Locate the Plasmodium falciparum-infected red blood cells and any of indeterminate infection status.
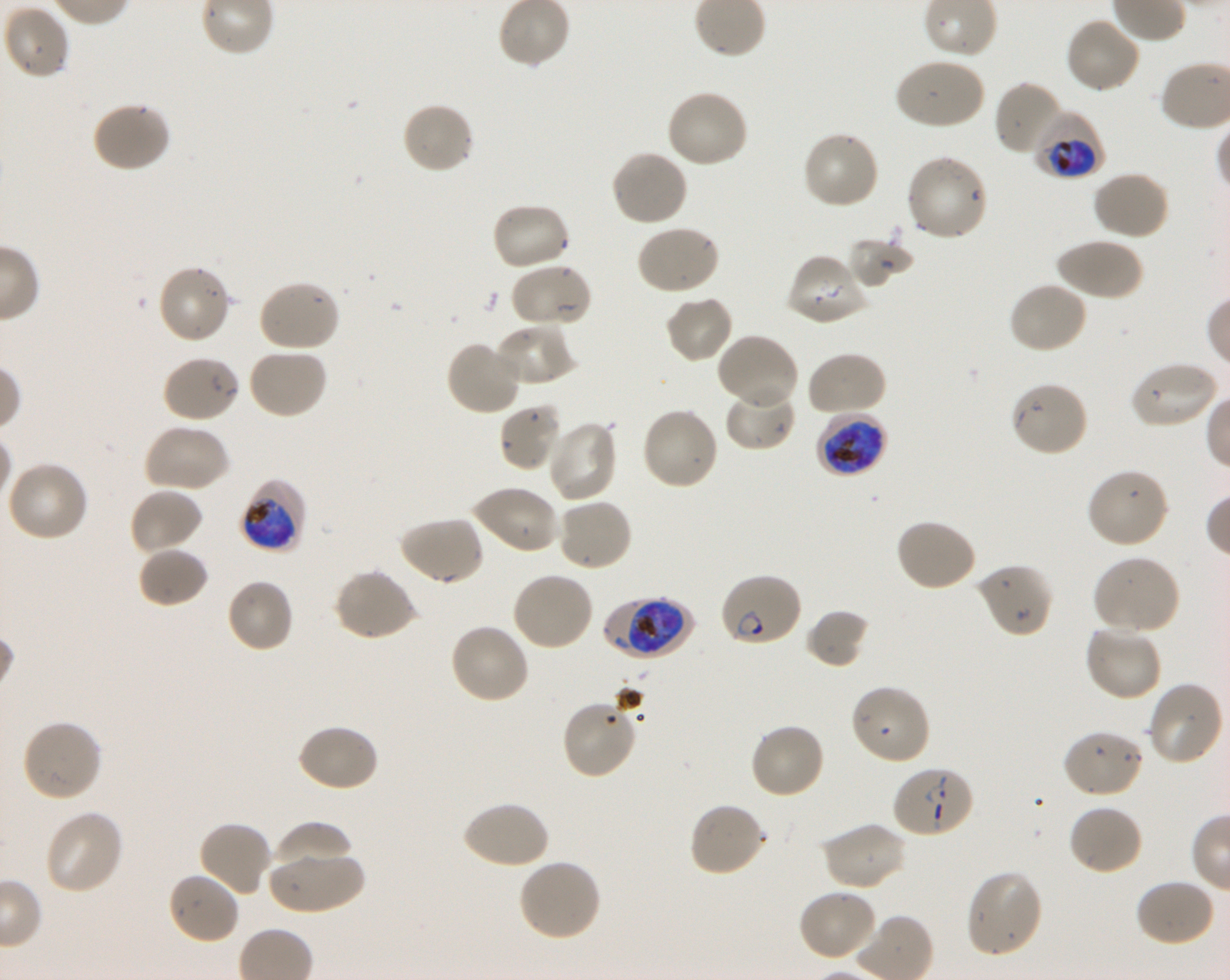
Approximate bounding rectangles given as corner coordinates in pixels from the top-left. Not every red blood cell is marked. A life-cycle stage — or a range of stages, where the recorded stages span more than one — follows each staged infected red blood cell.
Infected red blood cells: (x1=1032, y1=110, x2=1108, y2=180) trophozoite; (x1=815, y1=411, x2=888, y2=478) late trophozoite to late schizont; (x1=240, y1=482, x2=305, y2=551) early trophozoite to early schizont; (x1=717, y1=572, x2=802, y2=648) ring; (x1=603, y1=594, x2=693, y2=660) early trophozoite to early schizont; (x1=891, y1=764, x2=975, y2=839) ring.
No red blood cells of indeterminate infection status observed.

Summary:
  - Locations of uninfected red blood cells: (x1=3, y1=4, x2=70, y2=80), (x1=1064, y1=15, x2=1142, y2=95), (x1=894, y1=57, x2=986, y2=131), (x1=993, y1=80, x2=1065, y2=157), (x1=665, y1=90, x2=750, y2=169), (x1=92, y1=101, x2=172, y2=174), (x1=401, y1=101, x2=475, y2=176), (x1=800, y1=131, x2=881, y2=211), (x1=610, y1=149, x2=689, y2=228), (x1=905, y1=154, x2=988, y2=242), (x1=1091, y1=170, x2=1170, y2=241), (x1=489, y1=202, x2=572, y2=272), (x1=636, y1=224, x2=721, y2=296), (x1=1055, y1=236, x2=1143, y2=302), (x1=847, y1=237, x2=914, y2=288), (x1=785, y1=251, x2=870, y2=326), (x1=510, y1=263, x2=593, y2=330), (x1=156, y1=264, x2=232, y2=345), (x1=257, y1=279, x2=341, y2=353), (x1=1007, y1=281, x2=1089, y2=355), (x1=664, y1=293, x2=734, y2=364), (x1=493, y1=324, x2=574, y2=386), (x1=716, y1=333, x2=800, y2=411), (x1=446, y1=339, x2=523, y2=416), (x1=246, y1=348, x2=329, y2=420), (x1=805, y1=351, x2=887, y2=418), (x1=160, y1=354, x2=240, y2=424), (x1=1127, y1=360, x2=1219, y2=430), (x1=1009, y1=380, x2=1090, y2=457), (x1=724, y1=385, x2=796, y2=451), (x1=498, y1=401, x2=565, y2=473), (x1=640, y1=406, x2=721, y2=492), (x1=545, y1=419, x2=619, y2=503), (x1=142, y1=424, x2=230, y2=493), (x1=5, y1=460, x2=89, y2=543), (x1=1087, y1=468, x2=1170, y2=549), (x1=469, y1=485, x2=559, y2=555), (x1=128, y1=487, x2=203, y2=555), (x1=555, y1=497, x2=633, y2=572), (x1=397, y1=515, x2=485, y2=586), (x1=894, y1=517, x2=977, y2=592), (x1=136, y1=545, x2=209, y2=608), (x1=1091, y1=555, x2=1181, y2=634), (x1=976, y1=562, x2=1054, y2=639), (x1=333, y1=568, x2=419, y2=642), (x1=510, y1=571, x2=595, y2=652), (x1=225, y1=578, x2=295, y2=653), (x1=806, y1=608, x2=870, y2=669), (x1=448, y1=621, x2=531, y2=705), (x1=1083, y1=623, x2=1163, y2=702), (x1=1146, y1=680, x2=1225, y2=766), (x1=849, y1=683, x2=932, y2=766), (x1=561, y1=698, x2=639, y2=780), (x1=21, y1=718, x2=103, y2=803), (x1=748, y1=722, x2=827, y2=800), (x1=295, y1=723, x2=379, y2=793), (x1=1061, y1=728, x2=1144, y2=798), (x1=460, y1=799, x2=550, y2=871), (x1=687, y1=801, x2=767, y2=879), (x1=1067, y1=803, x2=1143, y2=876), (x1=42, y1=808, x2=124, y2=896), (x1=197, y1=819, x2=273, y2=898), (x1=821, y1=820, x2=908, y2=891), (x1=271, y1=821, x2=352, y2=874), (x1=267, y1=851, x2=366, y2=914), (x1=517, y1=858, x2=602, y2=943), (x1=166, y1=870, x2=240, y2=945), (x1=964, y1=870, x2=1045, y2=959), (x1=1133, y1=878, x2=1216, y2=948), (x1=796, y1=888, x2=879, y2=962)
  - Life-cycle stages observed: ring, trophozoite
  - Stain: Giemsa
  - Donor blood group: O+
  - Culture: shaking in-vitro Plasmodium falciparum strain 3D7
  - Field of view: single
  - Image size: 1230×980 pixels
  - Preparation: thin blood smear
  - Objective: 100x, oil immersion, numerical aperture 1.30